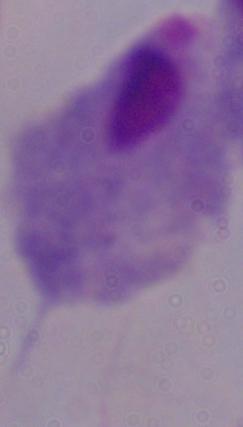 1000x magnification. A trichomonad is seen. Photomicrograph.